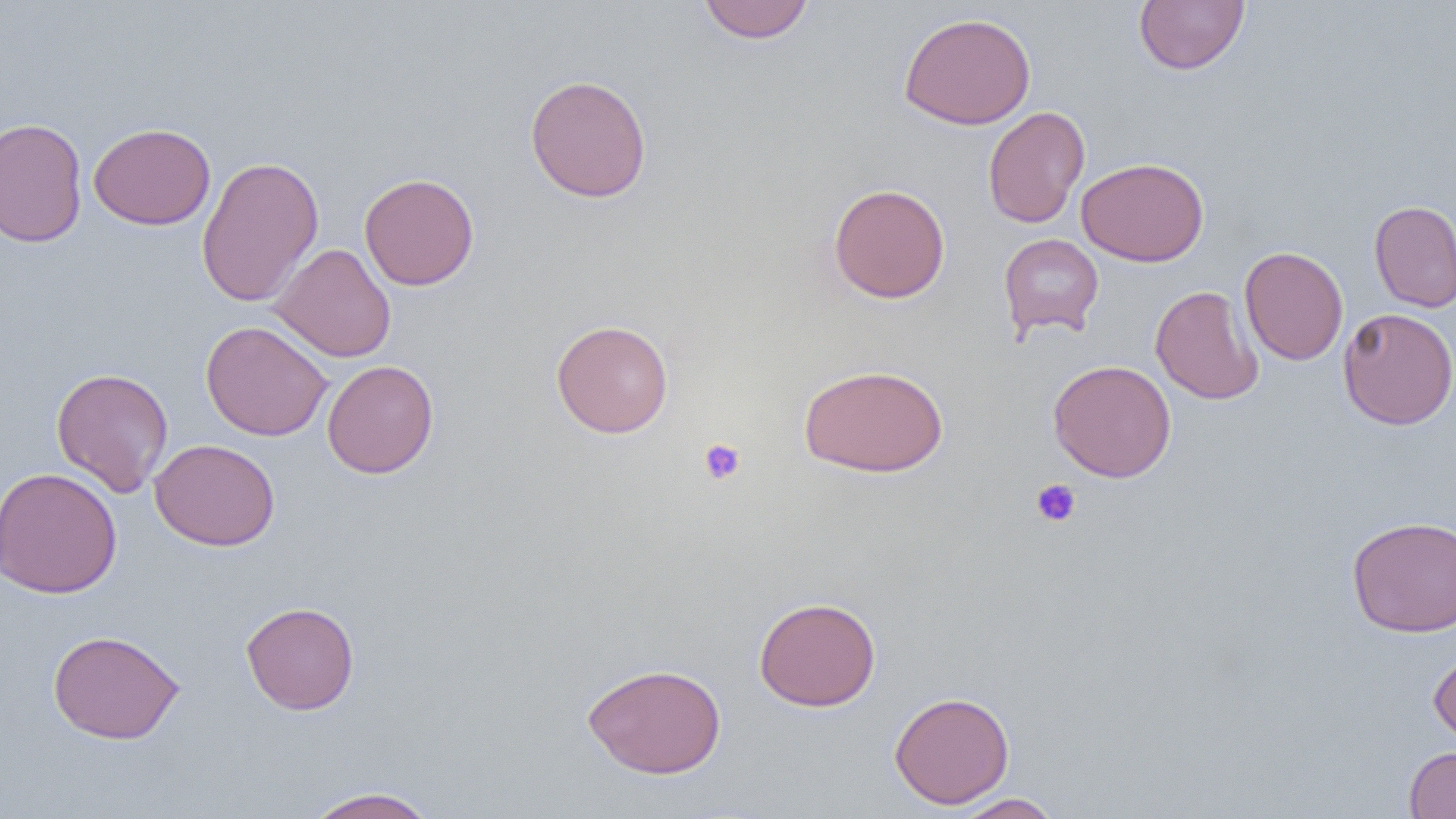
Approximate bounding boxes as named x1/y1/x2/y2 corners in pixels. Uninfected red blood cell locations: (x1=697, y1=0, x2=815, y2=44), (x1=1134, y1=0, x2=1249, y2=75), (x1=898, y1=12, x2=1036, y2=129), (x1=524, y1=74, x2=652, y2=203), (x1=982, y1=106, x2=1090, y2=229), (x1=0, y1=117, x2=88, y2=248), (x1=88, y1=122, x2=216, y2=230), (x1=196, y1=155, x2=324, y2=308), (x1=1076, y1=158, x2=1209, y2=267), (x1=359, y1=172, x2=479, y2=290), (x1=828, y1=183, x2=951, y2=304), (x1=1368, y1=200, x2=1456, y2=313), (x1=998, y1=233, x2=1104, y2=340), (x1=269, y1=243, x2=396, y2=362), (x1=1239, y1=246, x2=1348, y2=366), (x1=1150, y1=285, x2=1264, y2=405), (x1=1338, y1=307, x2=1456, y2=431), (x1=551, y1=319, x2=674, y2=438), (x1=200, y1=321, x2=333, y2=441), (x1=322, y1=359, x2=439, y2=479), (x1=1048, y1=359, x2=1176, y2=483), (x1=798, y1=363, x2=949, y2=478), (x1=50, y1=367, x2=174, y2=497), (x1=149, y1=439, x2=280, y2=552), (x1=1, y1=467, x2=123, y2=598), (x1=1346, y1=515, x2=1456, y2=637), (x1=753, y1=596, x2=881, y2=712), (x1=241, y1=601, x2=359, y2=715), (x1=47, y1=629, x2=185, y2=745), (x1=1428, y1=649, x2=1456, y2=748), (x1=583, y1=663, x2=727, y2=778), (x1=888, y1=690, x2=1015, y2=809), (x1=1404, y1=746, x2=1456, y2=819), (x1=303, y1=786, x2=441, y2=819), (x1=951, y1=793, x2=1064, y2=818). Platelet locations: (x1=698, y1=438, x2=746, y2=485), (x1=1031, y1=478, x2=1081, y2=527). Slide-level diagnosis: no evidence of blood parasites. Single field of view. Light microscopy. Thin blood film. Captured at 1000x magnification. Image is 1456×819 pixels.